Locate every leukocyte (white blood cell).
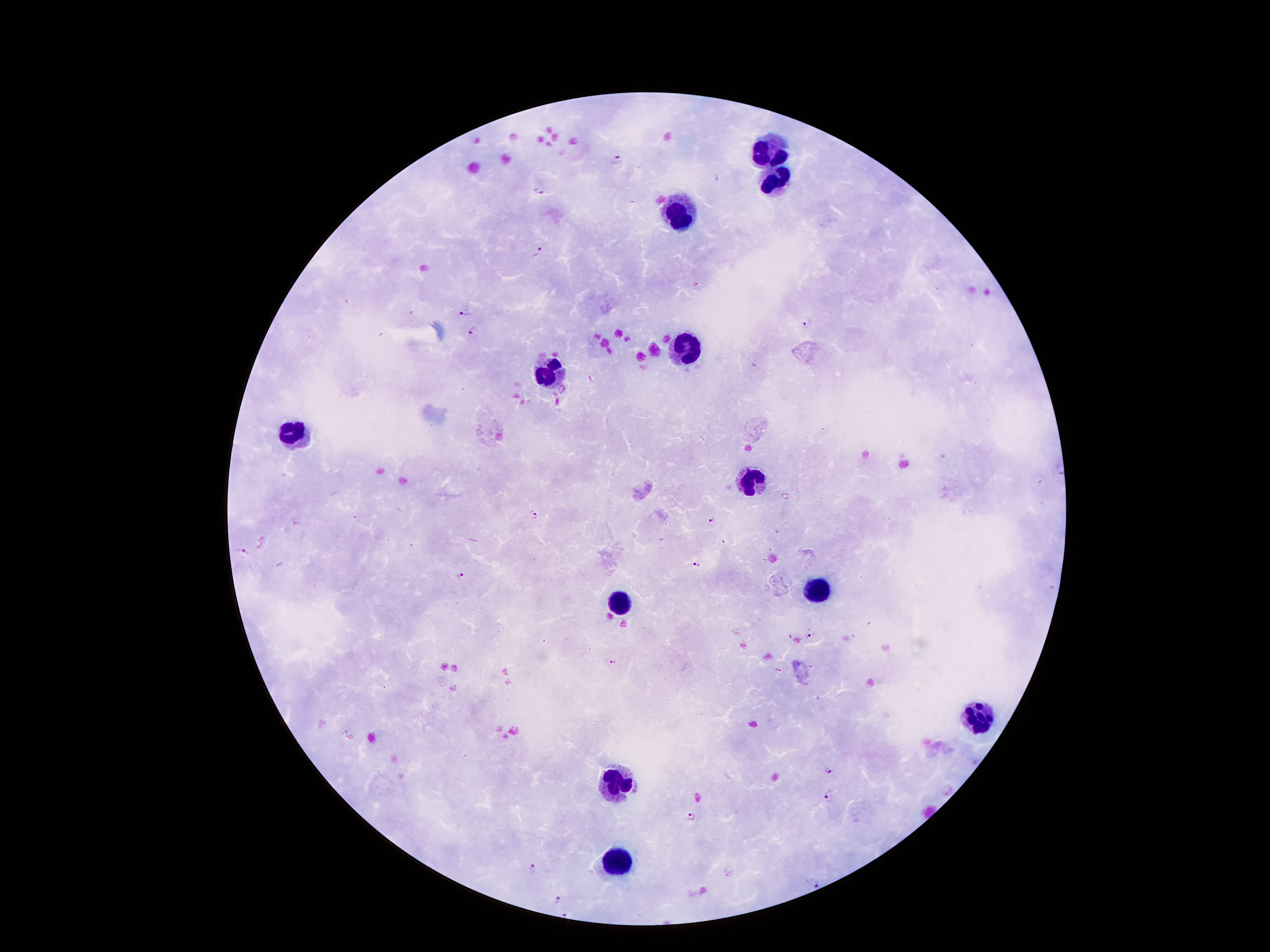

Approximate object centers, in pixels from the top-left corner.
Leukocytes: (x=767, y=153), (x=777, y=179), (x=679, y=216), (x=685, y=347), (x=551, y=374), (x=293, y=433), (x=750, y=481), (x=813, y=590), (x=620, y=605), (x=977, y=718), (x=614, y=785), (x=618, y=863).

Malaria parasite locations: (x=617, y=158), (x=540, y=189), (x=538, y=251), (x=466, y=310), (x=807, y=322), (x=472, y=331), (x=531, y=515), (x=712, y=521), (x=243, y=550), (x=696, y=564), (x=458, y=575), (x=809, y=635), (x=612, y=661), (x=827, y=769), (x=829, y=795), (x=691, y=815), (x=531, y=868), (x=814, y=883), (x=558, y=900), (x=566, y=914). Giemsa stain. 100x magnification. Thick peripheral-blood smear. Smartphone photograph taken through the microscope eyepiece. Single field of view. Patient malaria status: positive for Plasmodium falciparum. Image is 1270×952 pixels.